Assess this cell for malaria.
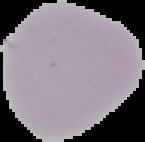

It is uninfected.

Segmented cell region on a black background. From a thin blood film. Image is 145×142 pixels.